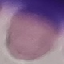

Summary:
  - Result: no malaria parasites seen
  - Preparation: thin smear
  - Capture: smartphone through the microscope eyepiece
  - Stain: Giemsa
  - Image type: automatically extracted cell patch, resized to 64 × 64 pixels